Classify this cell by malaria status.
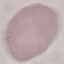
It is uninfected.

preparation = thin smear
image type = automatically extracted cell patch, resized to 64 × 64 pixels
capture = smartphone camera at the microscope eyepiece
stain = Giemsa